Assess this cell for malaria.
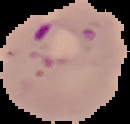
Parasitized.

Summary:
  - Image type: segmented cell region with the area outside set to black
  - Preparation: thin blood film
  - Image size: 130×124 pixels